Locate and identify every blood parasite.
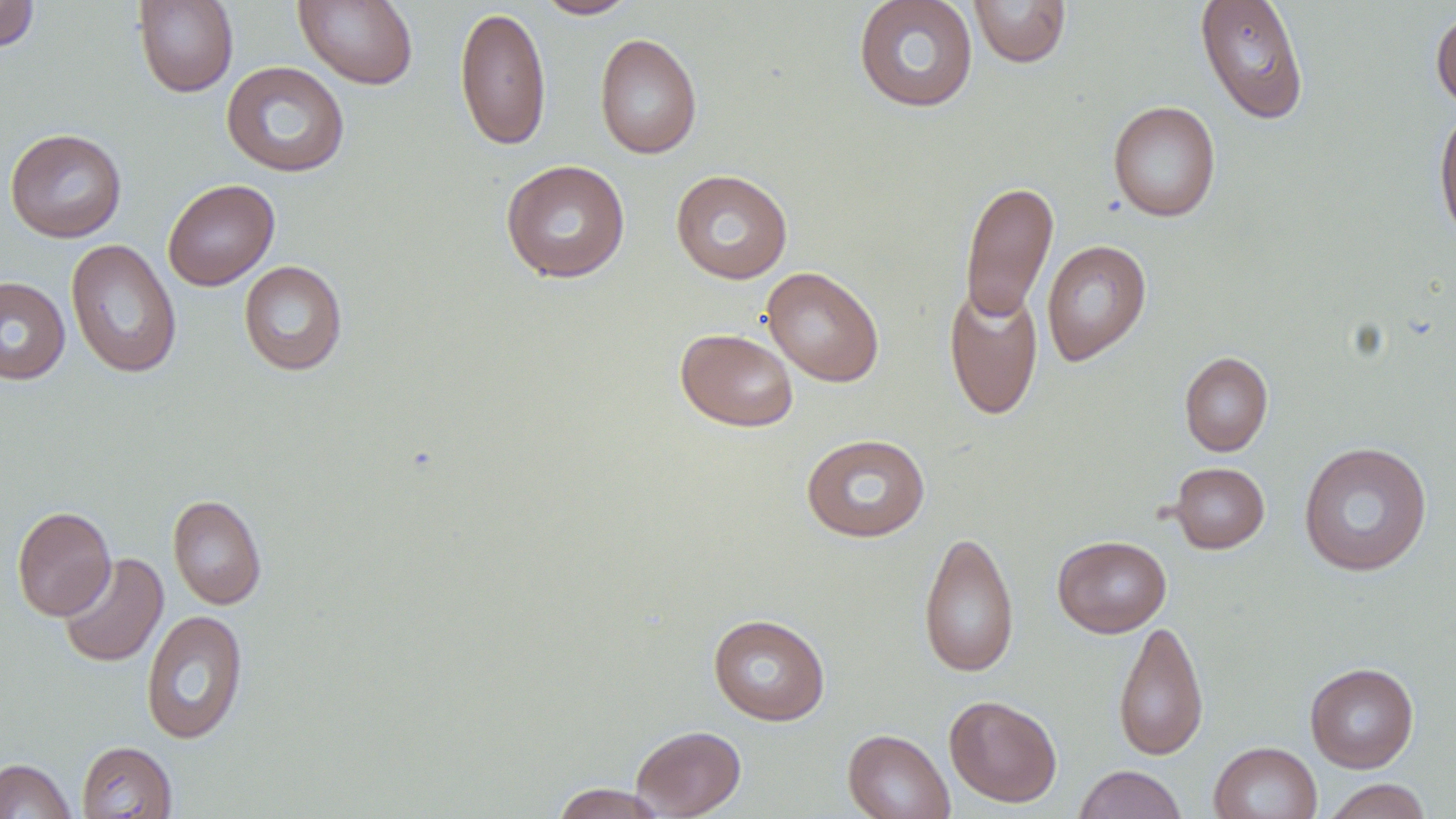
No blood parasites seen.

Approximate bounding boxes as [x1, y1, x2, y2] in pixels. Uninfected red blood cell locations: [0, 0, 40, 52], [133, 0, 238, 98], [293, 0, 419, 90], [535, 0, 639, 19], [852, 0, 979, 113], [968, 0, 1072, 68], [1194, 1, 1310, 124], [455, 5, 551, 151], [1430, 7, 1456, 112], [594, 32, 703, 159], [220, 61, 350, 178], [1107, 100, 1221, 223], [1433, 105, 1456, 249], [5, 128, 127, 243], [500, 159, 630, 283], [670, 169, 793, 284], [162, 178, 280, 291], [960, 179, 1058, 322], [65, 238, 182, 378], [1041, 239, 1151, 366], [239, 260, 348, 376], [761, 267, 885, 386], [0, 276, 70, 385], [943, 282, 1043, 420], [675, 327, 798, 432], [1179, 351, 1273, 456], [800, 433, 931, 542], [1297, 441, 1433, 577], [1168, 462, 1270, 554], [168, 494, 266, 610], [12, 505, 115, 621], [918, 529, 1019, 679], [1052, 535, 1171, 638], [58, 552, 168, 668], [141, 609, 249, 745], [708, 613, 830, 725], [1112, 619, 1208, 760], [1305, 662, 1419, 773], [944, 694, 1062, 808], [630, 725, 746, 818], [842, 728, 955, 819], [76, 740, 177, 818], [1209, 741, 1322, 819], [0, 758, 77, 819], [1073, 764, 1188, 819], [1322, 778, 1433, 819], [548, 783, 669, 818]. Slide-level diagnosis: negative for blood parasites. Image is 1456×819 pixels. Optical microscopy. Thin blood smear. Single field of view. May-Grünwald-Giemsa-stained preparation. Captured at 1000x magnification.